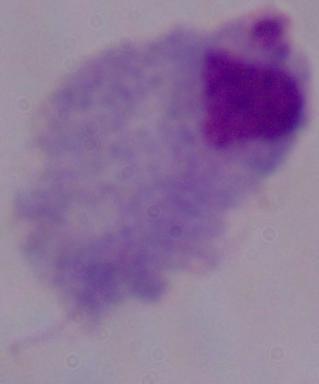
Micrograph. 1000x magnification. A trichomonad is shown.